Find each parasitized RBC.
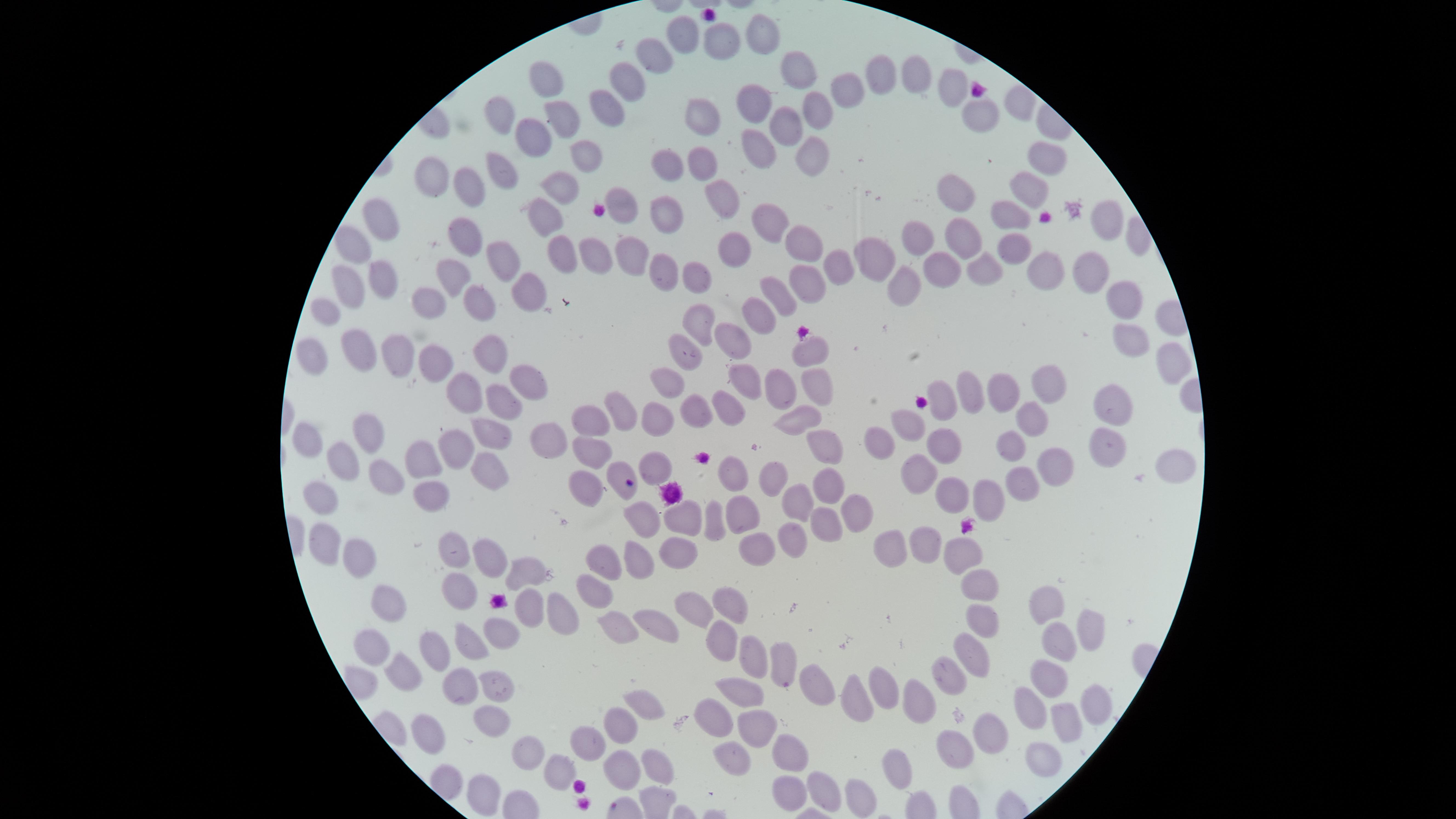
No parasitized RBCs identified.

Approximate marker points as (x, y) in pixels.
Summary:
  - Uninfected RBCs: (759, 35), (683, 36), (717, 40), (659, 54), (885, 70), (919, 71), (793, 72), (631, 73), (547, 76), (848, 86), (956, 88), (753, 97), (610, 101), (818, 101), (984, 112), (689, 114), (566, 115), (501, 119), (784, 126), (530, 136), (759, 149), (586, 150), (809, 150), (1050, 157), (703, 162), (501, 166), (666, 169), (430, 172), (465, 177), (558, 187), (1028, 187), (721, 194), (957, 195), (617, 205), (1010, 212), (669, 215), (391, 217), (1108, 217), (770, 218), (541, 220), (461, 233), (961, 236), (918, 237), (803, 238), (355, 239), (1011, 246), (734, 249), (873, 250), (499, 253), (558, 254), (588, 255), (635, 255), (940, 264), (1049, 264), (988, 268), (835, 270), (446, 271), (384, 272), (664, 273), (1087, 276), (352, 279), (692, 279), (903, 280), (809, 282), (526, 286), (777, 293), (1129, 295), (478, 299), (324, 305), (427, 305), (759, 315), (704, 317), (1130, 336), (734, 341), (313, 345), (352, 347), (396, 349), (496, 351), (808, 351), (687, 352), (428, 354), (1165, 356), (527, 373), (748, 377), (667, 378), (813, 382), (780, 385), (460, 387), (1050, 387), (1007, 389), (972, 394), (499, 399), (1114, 401), (944, 405), (727, 406), (689, 407), (622, 410), (1035, 413), (658, 415), (796, 416), (588, 418), (915, 419), (486, 432), (376, 433), (310, 439), (452, 440), (537, 440), (821, 440), (1102, 442), (939, 444), (1011, 444), (591, 445), (877, 445), (423, 457), (1057, 458), (343, 461), (486, 463), (1175, 463), (653, 465), (622, 466), (914, 468), (734, 469), (771, 475), (387, 476), (835, 478), (586, 479), (1030, 481), (954, 492), (432, 496), (987, 496), (320, 497), (791, 498), (744, 511), (855, 512), (680, 515), (646, 518), (717, 520), (825, 529), (783, 537), (322, 541), (923, 545), (456, 546), (753, 548), (896, 549), (357, 550), (966, 552), (491, 554), (674, 558), (602, 560), (633, 560), (525, 568), (977, 586), (458, 587), (597, 588), (727, 602), (389, 604), (1052, 607), (695, 608), (528, 610), (557, 611), (653, 620), (979, 622), (614, 626), (1088, 627), (502, 634), (717, 639), (373, 642), (1053, 643), (468, 644), (433, 646), (970, 651), (749, 657), (780, 663), (401, 669), (1044, 674), (941, 676), (464, 682), (497, 683), (888, 685), (809, 687), (741, 691), (850, 697), (916, 699), (642, 704), (1083, 705), (1034, 710), (716, 714), (491, 717), (1061, 719), (623, 726), (750, 727), (426, 732), (991, 735), (583, 736), (732, 754), (955, 754), (1039, 754), (531, 755), (789, 759), (557, 767), (618, 769), (900, 769), (655, 770), (826, 784), (788, 787), (478, 790), (862, 795)
  - Preparation: thin blood smear
  - Field of view: single
  - Capture: smartphone photograph through the microscope eyepiece
  - Stain: Giemsa
  - Visible region: circular
  - Image size: 1456×819 pixels